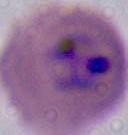

modality: micrograph
magnification: 400x or 1000x
identification: Plasmodium